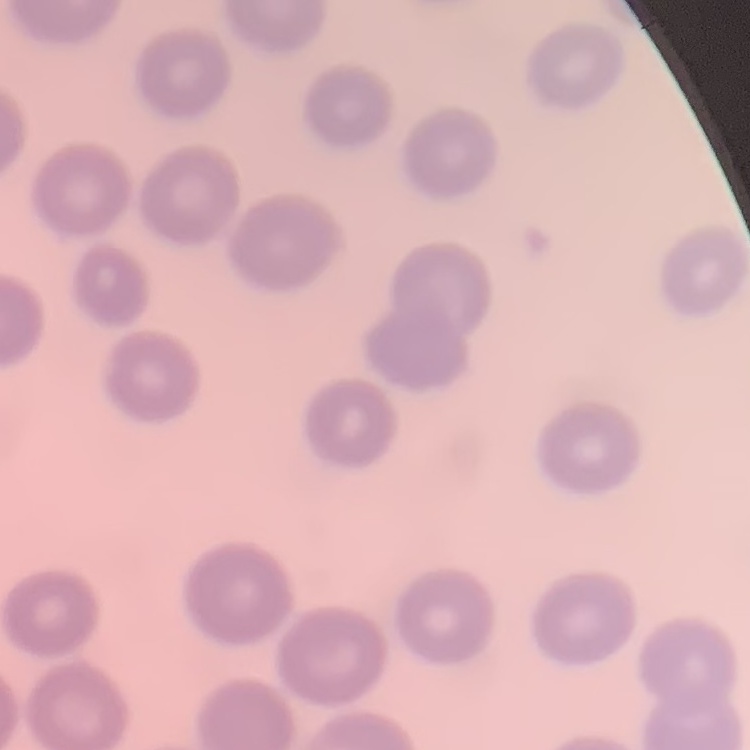
erythrocyte morphology = no rouleaux formation
image type = one tile cut from a larger photomicrograph
stain = Field's or Giemsa
preparation = thin blood film